Report the malaria status of this cell.
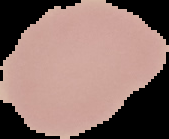

Uninfected.

Summary:
  - Preparation: thin blood smear
  - Image type: segmented cell region on a black background
  - Image size: 169×139 pixels